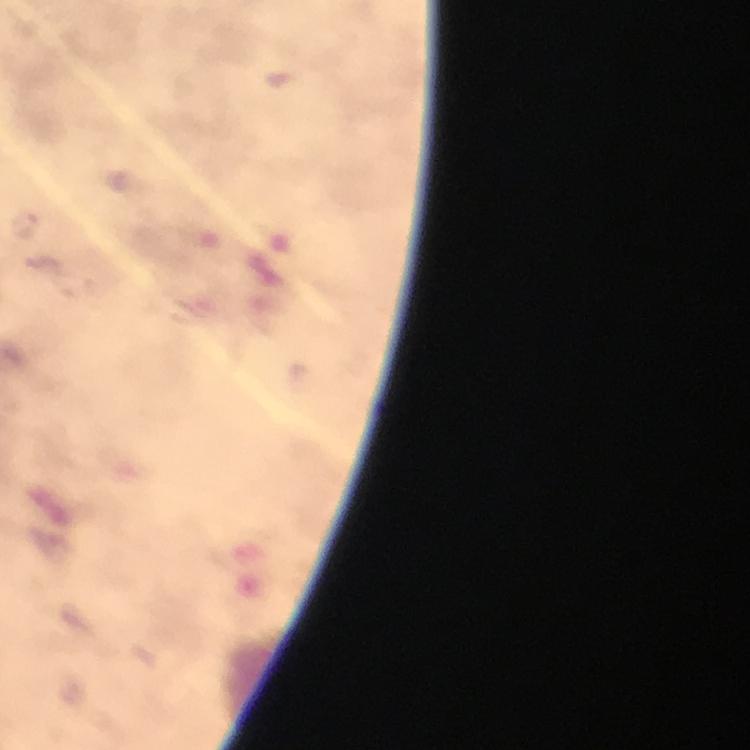
cropped from = a single field of view
capture = smartphone camera through the microscope
stain = Giemsa
preparation = thick blood film
image size = 750×750 pixels
immersion oil = used
Plasmodium parasite locations = approximate centers as (x, y) in pixels: (26, 223)
context = from a malaria diagnostic workup
magnification = 100x